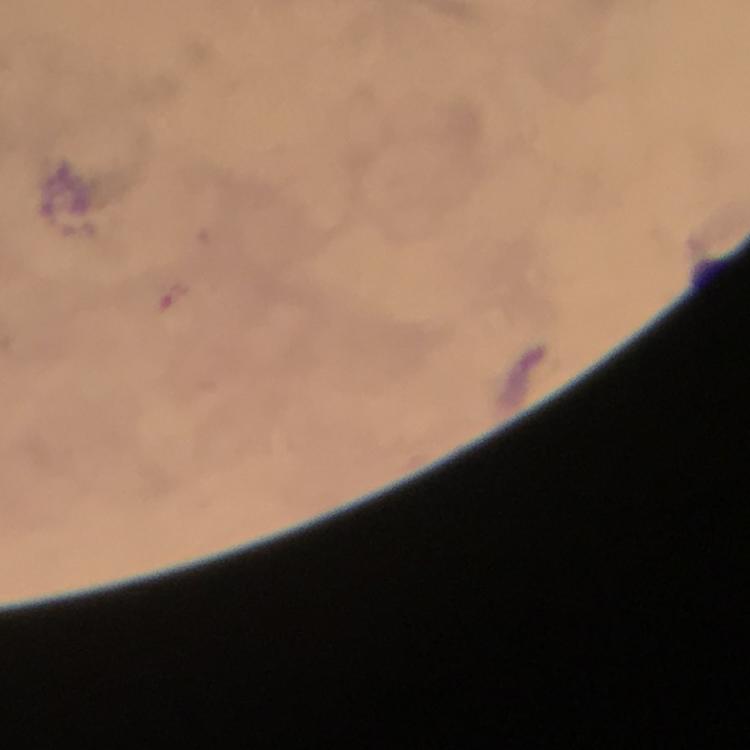
Approximate centers as (x, y) in pixels.
Summary:
  - Malaria parasite locations: (175, 295)
  - Context: from a malaria diagnostic workup
  - Magnification: 100x
  - Immersion oil: used
  - Preparation: thick blood film
  - Stain: Giemsa
  - Image size: 750×750 pixels
  - Cropped from: one field of view
  - Capture: smartphone photograph through a microscope